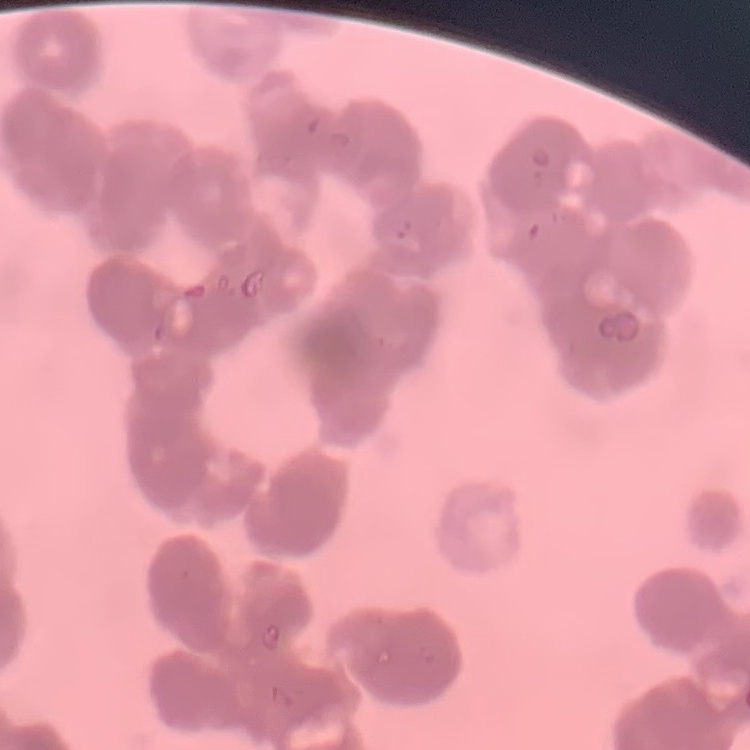 The erythrocytes exhibit rouleaux formation. Field's or Giemsa stain. Square crop of a larger photomicrograph. Thin blood film.